Locate platelets.
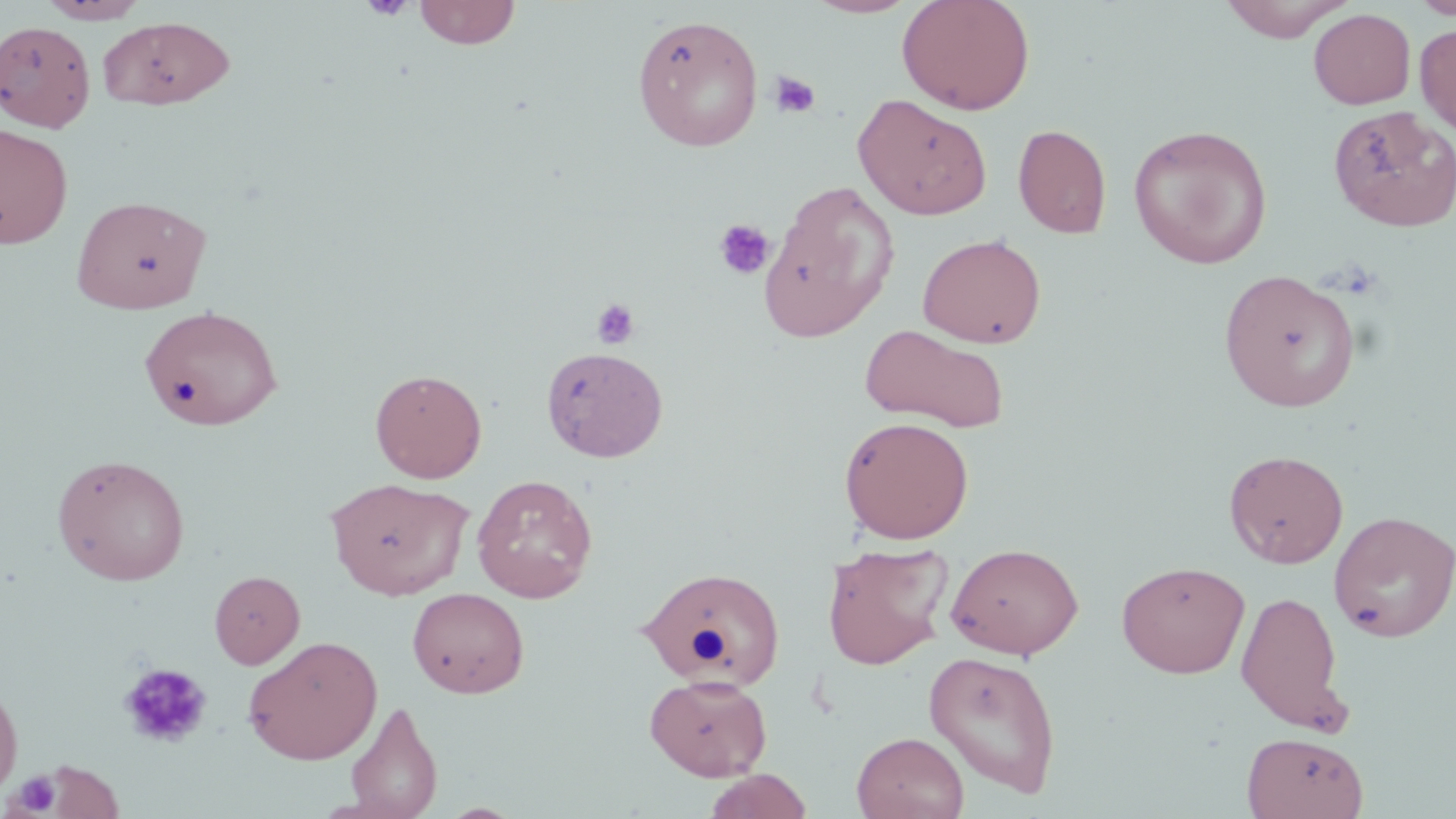

Approximate bounding boxes as (x1, y1, x2, y2) in pixels.
Platelets: (361, 0, 415, 21), (769, 71, 820, 118), (714, 218, 776, 281), (591, 298, 640, 350), (117, 662, 213, 750), (7, 771, 62, 816).

Uninfected red blood cell locations: (413, 0, 521, 49), (803, 0, 921, 18), (897, 0, 1035, 115), (1220, 0, 1353, 43), (1411, 0, 1456, 19), (39, 1, 148, 24), (1308, 8, 1416, 109), (632, 13, 763, 151), (98, 15, 234, 110), (0, 22, 95, 133), (1415, 23, 1456, 136), (852, 93, 993, 220), (1327, 105, 1455, 232), (0, 123, 73, 249), (1013, 123, 1112, 238), (1128, 124, 1273, 268), (760, 182, 899, 342), (72, 194, 212, 314), (917, 233, 1046, 348), (1218, 268, 1361, 412), (139, 305, 284, 431), (859, 324, 1011, 434), (542, 346, 668, 463), (370, 368, 487, 483), (839, 416, 974, 544), (1224, 449, 1349, 568), (52, 453, 191, 585), (471, 474, 598, 602), (326, 477, 473, 600), (1328, 510, 1456, 642), (821, 541, 954, 670), (946, 542, 1085, 659), (1116, 560, 1250, 678), (638, 566, 786, 691), (209, 570, 304, 668), (407, 587, 529, 699), (1236, 590, 1347, 732), (243, 635, 383, 764), (925, 649, 1062, 798), (645, 673, 772, 781), (0, 675, 24, 801), (343, 699, 443, 819), (852, 731, 969, 819), (1242, 732, 1368, 818), (41, 759, 124, 818), (702, 769, 814, 819). Slide-level diagnosis: negative for blood parasites. Captured at 1000x magnification. Light microscopy. Single field of view. May-Grünwald-Giemsa stain. Thin blood film. Image is 1456×819 pixels.